Assess this cell for malaria.
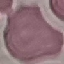
Uninfected.

Giemsa stain. Thin blood smear. Acquired by smartphone through the microscope eyepiece. Cell patch, automatically extracted from a larger field of view and resized to 64 × 64 pixels.